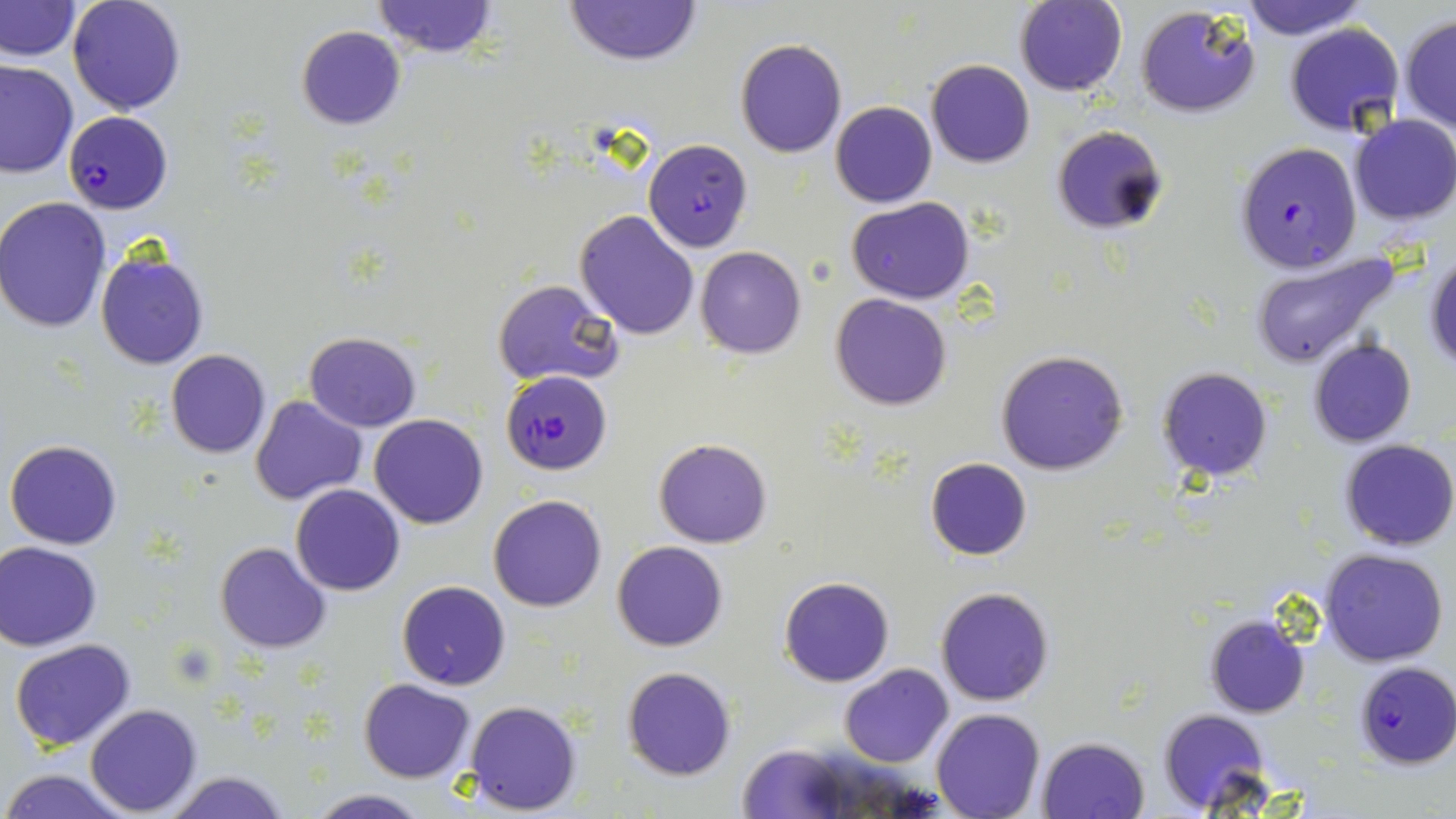

Summary:
  - Coordinate format: approximate bounding boxes as [x1, y1, x2, y2] in pixels
  - Plasmodium falciparum-infected red blood cell locations: [65, 110, 173, 213], [1234, 141, 1362, 273], [501, 370, 612, 474], [1355, 661, 1456, 768]
  - Uninfected red blood cell locations: [0, 0, 80, 61], [67, 0, 188, 115], [1015, 0, 1127, 96], [1239, 0, 1364, 39], [373, 1, 498, 57], [563, 1, 703, 66], [1135, 4, 1261, 119], [1399, 15, 1456, 136], [1285, 21, 1405, 137], [296, 27, 406, 130], [735, 38, 847, 157], [0, 60, 78, 179], [925, 60, 1034, 168], [830, 101, 937, 208], [1348, 114, 1456, 227], [1051, 124, 1168, 233], [643, 138, 753, 251], [0, 198, 111, 332], [847, 198, 975, 303], [569, 208, 695, 337], [695, 246, 805, 359], [95, 250, 210, 369], [1425, 251, 1456, 369], [1250, 252, 1400, 371], [494, 279, 621, 386], [831, 293, 951, 411], [304, 332, 422, 431], [1308, 338, 1418, 447], [995, 349, 1129, 476], [166, 350, 271, 458], [1156, 367, 1274, 481], [250, 395, 368, 505], [370, 413, 489, 528], [5, 438, 123, 550], [653, 438, 774, 548], [1339, 440, 1455, 551], [925, 457, 1032, 561], [291, 484, 405, 597], [487, 493, 607, 613], [612, 540, 728, 651], [1, 541, 103, 650], [215, 541, 332, 653], [1318, 548, 1449, 666], [779, 575, 894, 687], [397, 580, 511, 690], [935, 585, 1055, 706], [1203, 614, 1310, 717], [9, 640, 136, 751], [839, 663, 953, 767], [623, 666, 737, 780], [358, 678, 476, 783], [463, 700, 584, 814], [84, 704, 202, 816], [1159, 708, 1271, 813], [931, 709, 1044, 819], [1036, 735, 1150, 819], [733, 741, 861, 816], [2, 767, 133, 819], [164, 770, 292, 819], [306, 789, 428, 819]
  - Slide-level diagnosis: Plasmodium falciparum
  - Preparation: thin blood smear
  - Modality: optical microscopy
  - Stain: May-Grünwald-Giemsa
  - Magnification: 1000x
  - Field of view: single
  - Image size: 1456×819 pixels